Classify this cell by malaria status.
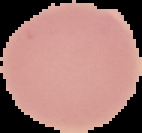
It is uninfected.

Summary:
  - Image type: segmented cell region with the area outside set to black
  - Image size: 142×133 pixels
  - Preparation: thin blood smear